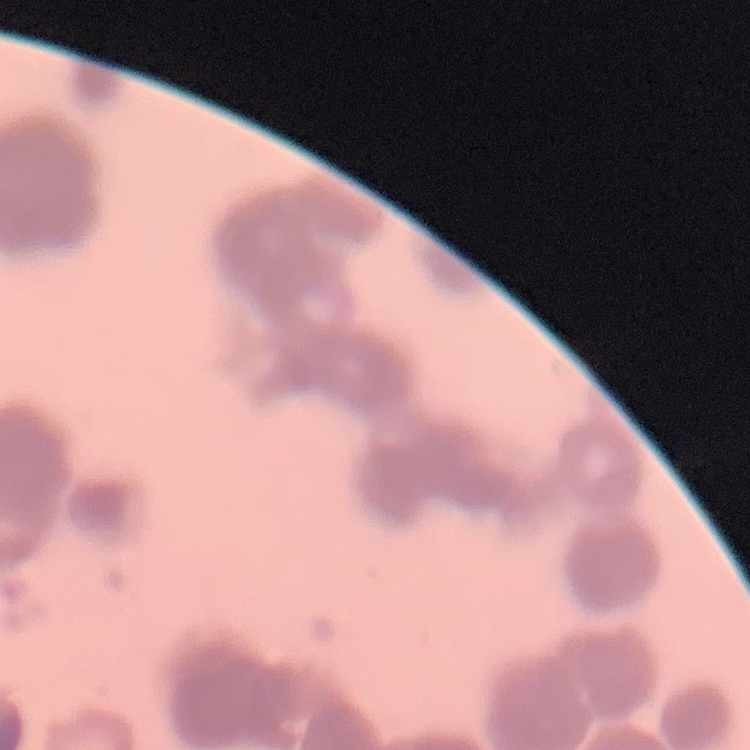
The red blood cells exhibit rouleaux formation. Thin peripheral smear. One tile cut from a larger photomicrograph. Stained with either Field's or Giemsa.